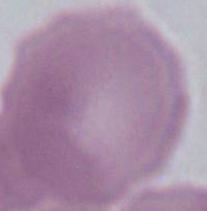

magnification = 1000x
identification = erythrocyte
modality = micrograph